Assess this cell for malaria.
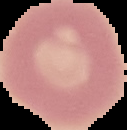

It is uninfected.

Summary:
  - Image size: 127×130 pixels
  - Preparation: thin blood smear
  - Image type: segmented cell region with the area outside set to black